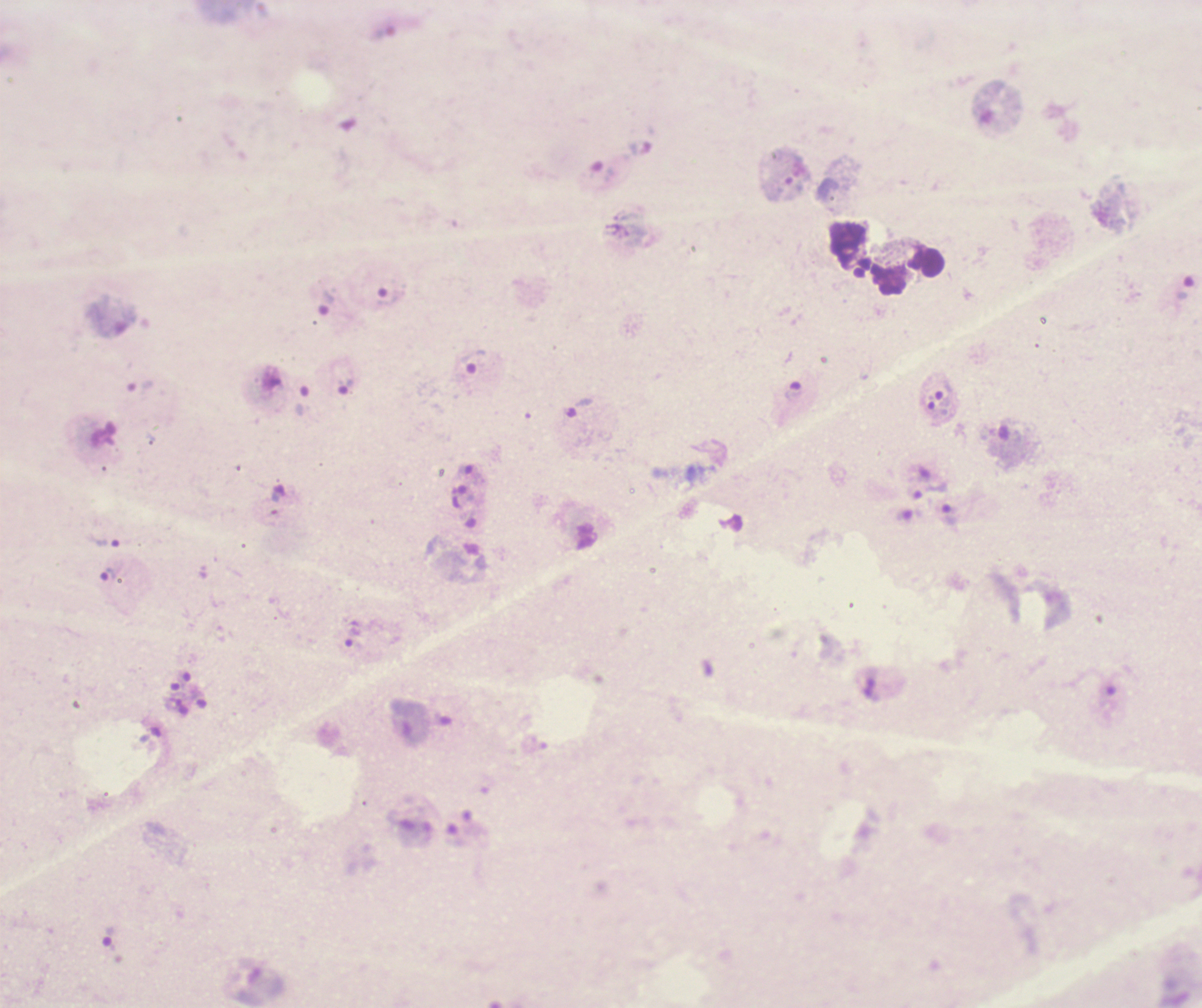
coordinate format = approximate centers as {x, y} in pixels
leukocyte locations = {909, 272}
trophozoite locations = {1186, 290}, {327, 302}, {473, 360}, {344, 387}, {794, 392}, {945, 395}, {303, 401}, {579, 408}, {930, 490}, {949, 516}, {104, 543}, {107, 576}
field of view = one from this slide
result = positive for Plasmodium parasites
stain = Romanowsky
context = previously used in a real diagnosis
coloration quality = bad
image size = 1202×1008 pixels
background quality = unsatisfactory
preparation = thick blood film
magnification = 100x